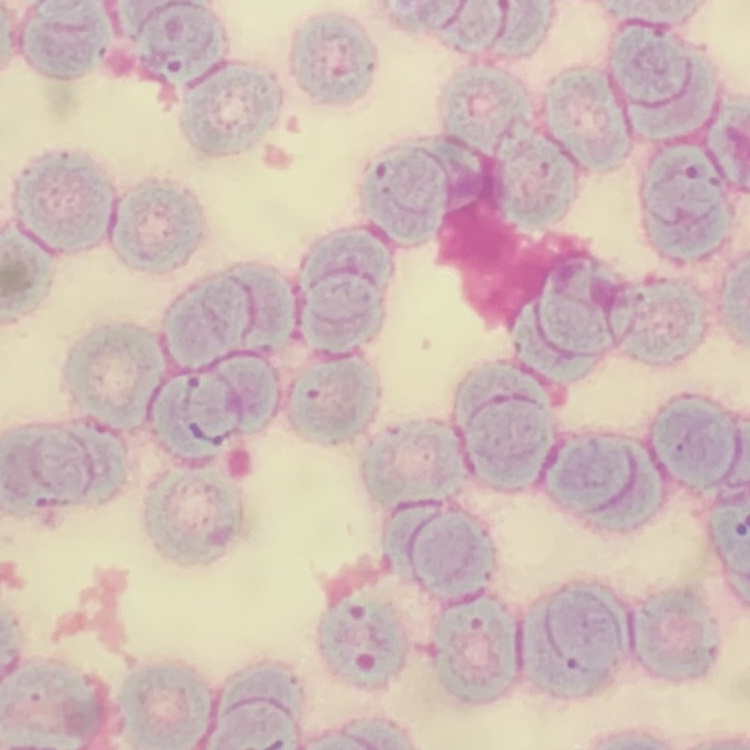

erythrocyte_morphology: rouleaux formation
stain: Field's or Giemsa
image_type: square crop of a larger photomicrograph
preparation: thin peripheral smear